Comment on the morphology of the red blood cells.
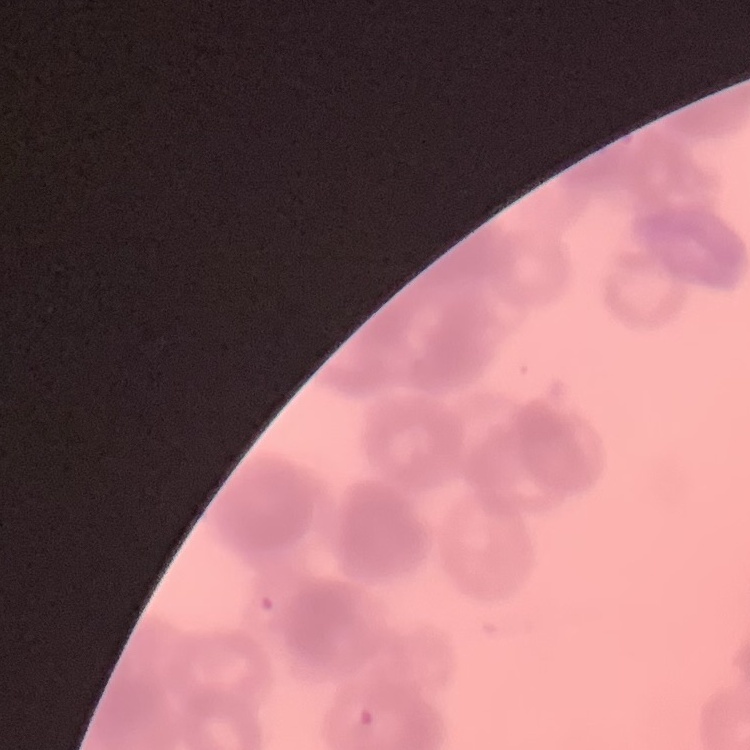

They show rouleaux formation.

preparation = thin peripheral smear
image type = one tile cut from a larger photomicrograph
stain = Field's or Giemsa